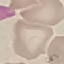

malaria status = uninfected
stain = Giemsa
preparation = thin blood smear
capture = smartphone through the microscope eyepiece
image type = automatically extracted cell patch, resized to 64 × 64 pixels